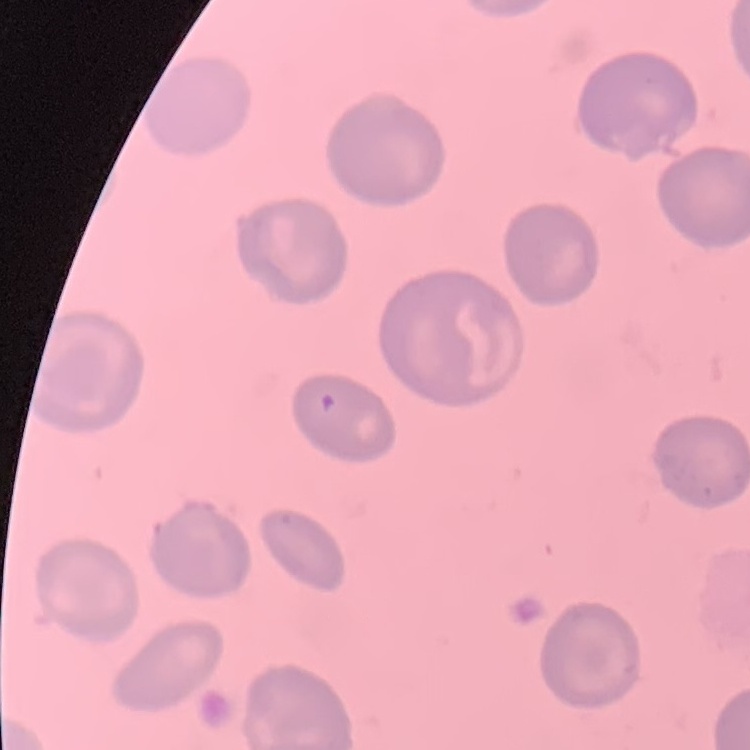

Summary:
  - Red blood cell morphology: no rouleaux formation
  - Image type: square crop of a larger photomicrograph
  - Stain: Field's or Giemsa
  - Preparation: thin peripheral smear